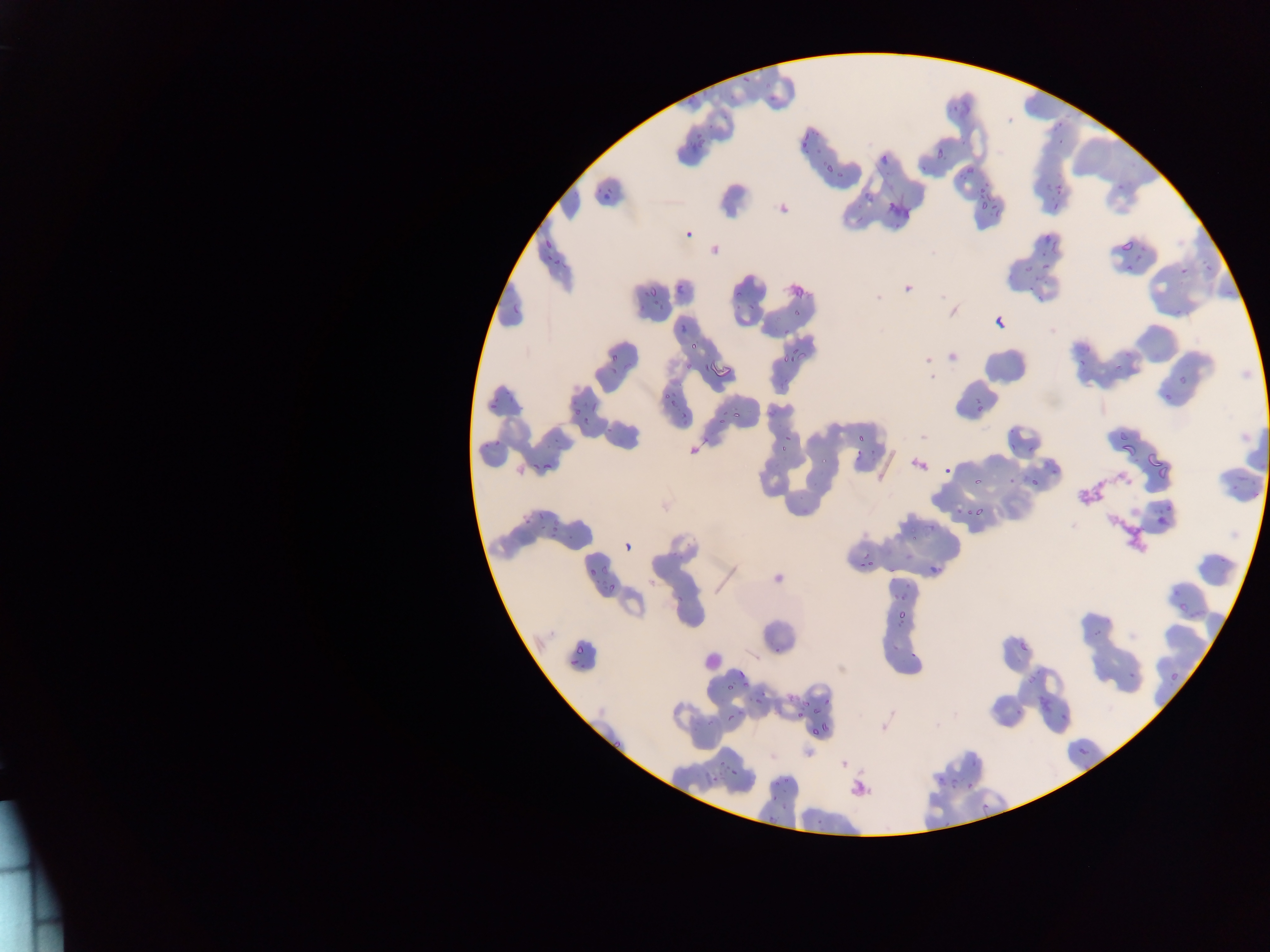

Approximate bounding boxes as {left, top, right, bottom} in pixels. Malaria parasite locations (subset; some below the resolvable size): {743, 74, 748, 84}, {803, 132, 813, 142}, {697, 136, 706, 149}, {803, 141, 808, 152}, {936, 145, 946, 157}, {827, 164, 834, 173}, {966, 169, 974, 172}, {1056, 180, 1063, 191}, {606, 188, 615, 195}, {1052, 199, 1059, 211}, {980, 200, 988, 210}, {992, 201, 998, 210}, {994, 209, 1004, 217}, {1044, 230, 1053, 244}, {1121, 236, 1137, 252}, {1050, 238, 1060, 256}, {544, 240, 553, 251}, {1042, 250, 1048, 258}, {1043, 263, 1052, 269}, {1025, 264, 1033, 272}, {1180, 268, 1188, 276}, {1205, 268, 1214, 275}, {650, 285, 657, 297}, {678, 285, 685, 295}, {514, 302, 519, 314}, {795, 308, 803, 315}, {996, 315, 1006, 330}, {681, 325, 685, 334}, {783, 328, 791, 336}, {689, 341, 696, 352}, {791, 348, 800, 356}, {800, 351, 808, 359}, {611, 353, 618, 363}, {785, 354, 789, 365}, {790, 355, 796, 364}, {1080, 358, 1085, 366}, {1114, 361, 1123, 371}, {684, 363, 693, 371}, {701, 363, 712, 374}, {670, 399, 677, 409}, {591, 401, 598, 412}, {975, 405, 983, 410}, {576, 407, 581, 418}, {722, 408, 729, 416}, {681, 411, 689, 419}, {731, 411, 740, 417}, {583, 417, 591, 423}, {719, 417, 729, 424}, {1119, 432, 1127, 441}, {857, 433, 863, 443}, {1009, 440, 1015, 452}, {779, 445, 787, 451}, {1122, 445, 1138, 453}, {1148, 453, 1159, 467}, {822, 456, 827, 464}, {534, 461, 541, 470}, {544, 464, 552, 469}, {1158, 465, 1167, 480}, {973, 478, 983, 489}, {973, 508, 984, 516}, {538, 511, 542, 520}, {554, 516, 560, 527}, {911, 536, 920, 541}, {861, 561, 864, 569}, {929, 565, 940, 573}, {589, 567, 595, 578}, {608, 585, 614, 593}, {901, 593, 906, 602}, {1180, 604, 1189, 612}, {900, 611, 908, 618}, {896, 621, 906, 626}, {1092, 628, 1102, 636}, {892, 640, 907, 651}, {1020, 643, 1028, 655}, {576, 644, 584, 653}, {773, 647, 782, 654}, {568, 659, 580, 666}, {738, 669, 746, 679}, {1126, 670, 1136, 680}, {1027, 673, 1035, 684}, {742, 679, 751, 691}, {724, 683, 734, 689}, {760, 691, 768, 696}, {1037, 695, 1052, 712}, {754, 700, 762, 705}, {824, 700, 832, 703}, {802, 701, 811, 707}, {1014, 708, 1024, 715}, {738, 709, 744, 717}, {814, 709, 817, 717}, {728, 712, 735, 721}, {797, 713, 805, 717}, {1061, 713, 1069, 723}, {707, 720, 713, 728}, {821, 723, 828, 731}, {811, 726, 818, 736}, {1075, 744, 1093, 759}, {719, 759, 729, 770}, {729, 770, 737, 775}, {950, 773, 957, 786}, {713, 775, 721, 782}, {938, 778, 946, 787}, {964, 780, 975, 791}, {772, 781, 781, 788}, {773, 793, 778, 801}, {780, 800, 788, 811}, {818, 813, 826, 825}, {767, 817, 777, 823} | approximate {x, y} pixel centers of objects too small to bound: {767, 86}, {772, 98}, {956, 108}, {1061, 125}, {1061, 142}, {962, 178}, {986, 184}, {1121, 188}, {981, 189}, {549, 257}, {556, 262}, {646, 295}, {655, 303}, {641, 307}, {661, 307}, {614, 369}, {666, 396}, {511, 399}, {494, 406}, {686, 423}, {609, 430}, {788, 437}, {873, 452}, {1013, 480}, {1034, 482}, {958, 512}, {968, 513}, {543, 528}, {553, 534}, {866, 556}, {872, 564}, {896, 596}, {680, 599}, {785, 781}. Leukocyte locations: {705, 649, 724, 673}. Thin blood smear. Image is 1270×952 pixels. Mobile-phone photograph taken through the microscope. One field of view. Collected in Ghana.